Outline each blood parasite and name the species.
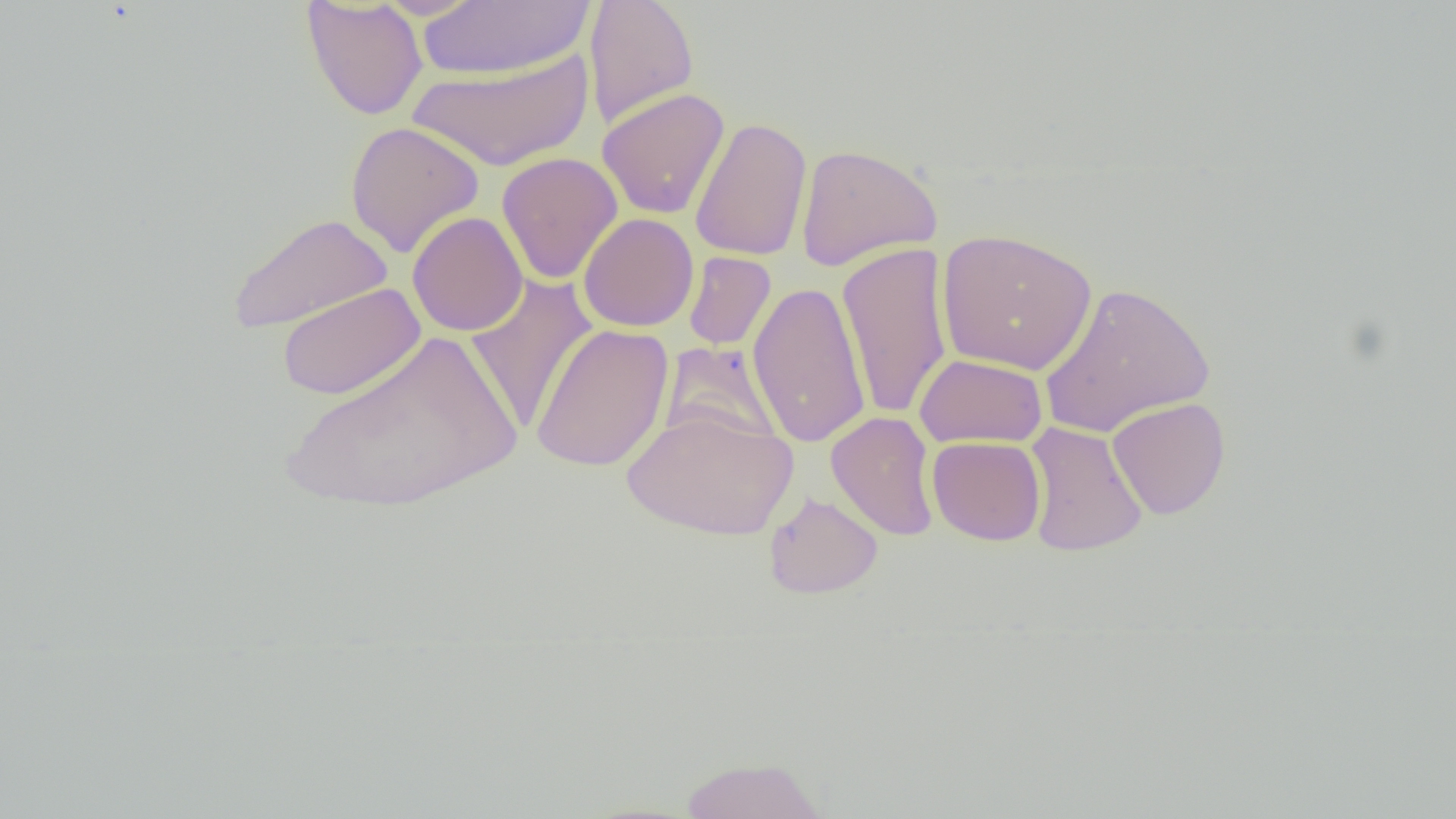
No blood parasites seen.

Approximate bounding boxes as (x1, y1, x2, y2) in pixels. Uninfected red blood cell locations: (301, 0, 428, 121), (372, 0, 487, 20), (583, 0, 699, 130), (414, 1, 595, 80), (407, 49, 595, 171), (597, 87, 730, 220), (689, 116, 812, 262), (345, 120, 485, 258), (794, 142, 944, 272), (496, 152, 623, 284), (407, 211, 528, 337), (228, 213, 393, 335), (578, 213, 699, 332), (936, 227, 1098, 376), (837, 243, 954, 420), (683, 251, 776, 351), (464, 274, 599, 435), (747, 280, 871, 449), (1038, 281, 1214, 437), (276, 282, 426, 401), (530, 323, 674, 472), (281, 329, 523, 517), (659, 342, 783, 450), (915, 353, 1048, 448), (1106, 397, 1231, 520), (622, 408, 798, 541), (826, 411, 940, 541), (1023, 421, 1148, 557), (927, 436, 1046, 546), (763, 491, 884, 600), (678, 756, 830, 819). Slide-level diagnosis: no evidence of blood parasites. Single field of view. Light microscopy. Captured at 1000x magnification. Thin blood film. Image is 1456×819 pixels.